Assess this cell for malaria.
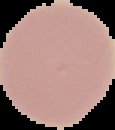

It is uninfected.

Segmented cell region on a black background. From a thin blood film. Image is 115×130 pixels.